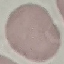

Summary:
  - Result: no malaria parasites seen
  - Capture: smartphone through the microscope eyepiece
  - Stain: Giemsa
  - Image type: automatically extracted cell patch, resized to 64 × 64 pixels
  - Preparation: thin smear